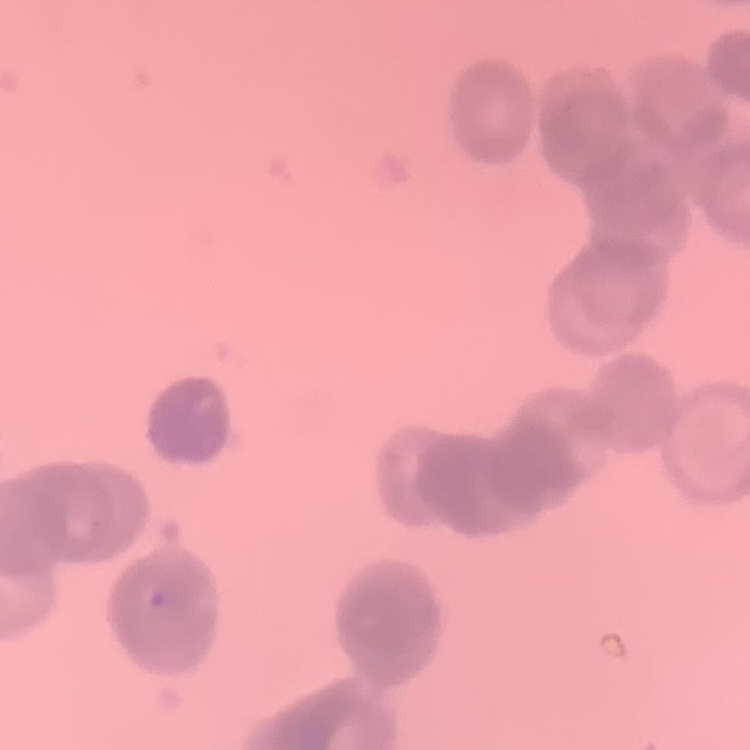 The erythrocytes show rouleaux formation. Thin blood film. One tile cut from a larger photomicrograph. Stained with either Field's or Giemsa.